Name the parasite shown.
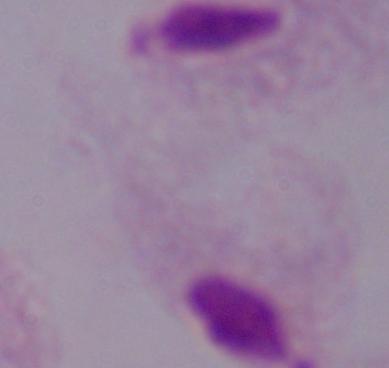

A trichomonad.

Summary:
  - Modality: micrograph
  - Magnification: 1000x